Assess this cell for malaria.
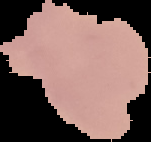
Uninfected.

{
  "preparation": "thin blood smear",
  "image_size": "151×142 pixels",
  "image_type": "segmented cell region with the area outside set to black"
}